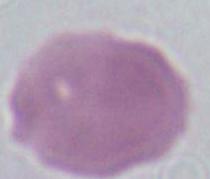
Summary:
  - Modality: photomicrograph
  - Identification: erythrocyte
  - Magnification: 1000x